State which parasite is depicted.
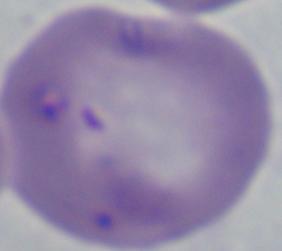
Babesia.

Summary:
  - Magnification: 1000x
  - Modality: photomicrograph